Classify this cell by malaria status.
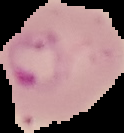

It is parasitized.

image size = 124×133 pixels
image type = segmented cell region on a black background
preparation = thin blood smear